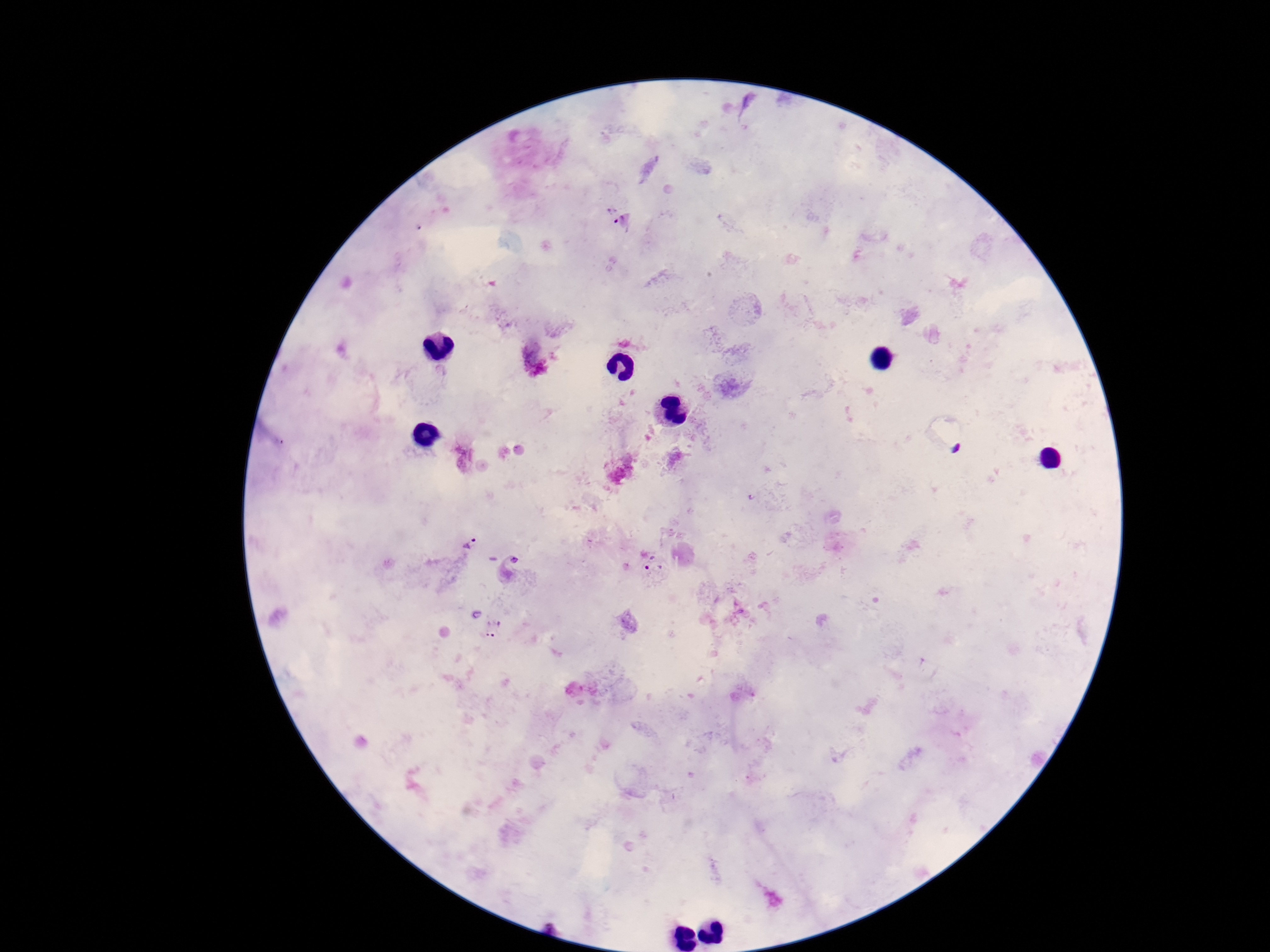

patient malaria status = infected
image size = 1270×952 pixels
Plasmodium parasite locations = approximate centers as (x, y) in pixels: (614, 216), (469, 543), (654, 570), (493, 627)
field of view = one from this slide
stain = Giemsa
capture = smartphone camera through the microscope eyepiece
magnification = 100x
preparation = thick blood film